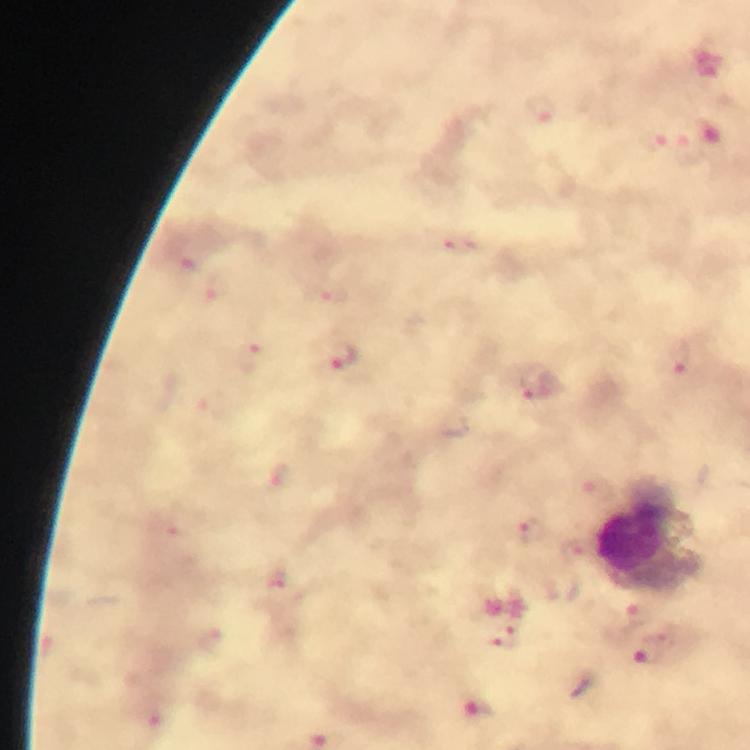

cropped_from: one field of view
immersion_oil: applied
leukocyte_locations: 'approximate object centers, in pixels from the top-left corner: (x=648, y=537)'
image_size: 750×750 pixels
preparation: thick blood film
magnification: 100x
malaria_parasite_locations: 'approximate object centers, in pixels from the top-left corner: (x=541, y=109), (x=456, y=244), (x=192, y=257), (x=216, y=287), (x=333, y=296), (x=342, y=355), (x=681, y=359), (x=249, y=360), (x=531, y=385), (x=595, y=490), (x=531, y=528), (x=579, y=553), (x=275, y=584), (x=638, y=613), (x=505, y=637), (x=648, y=654), (x=151, y=711), (x=478, y=711)'
stain: Giemsa
context: from a diagnostic examination for malaria
capture: smartphone camera through the microscope